Assess this cell for malaria.
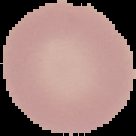
Uninfected.

Summary:
  - Image size: 136×136 pixels
  - Image type: segmented cell region on a black background
  - Preparation: thin blood smear